Comment on the morphology of the erythrocytes.
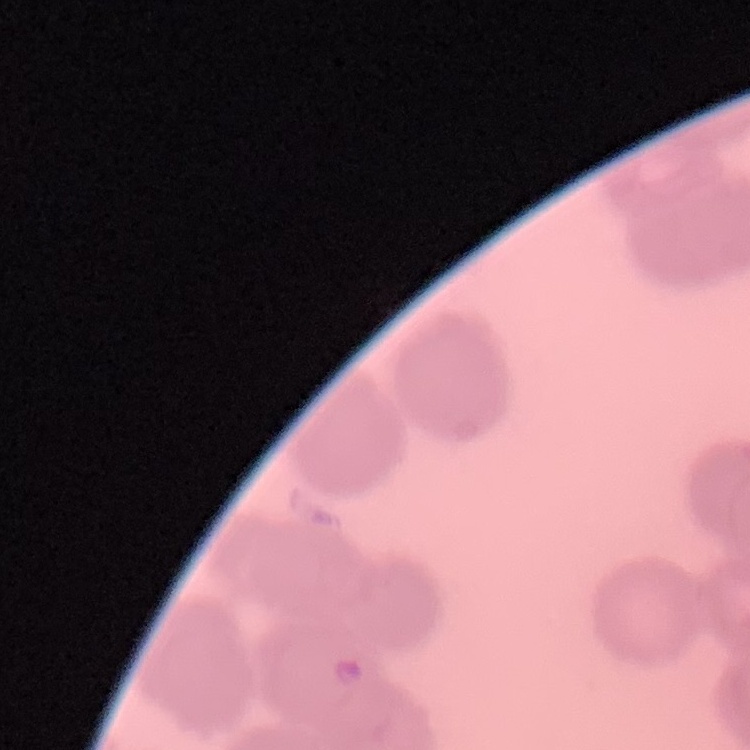
Rouleaux formation.

Summary:
  - Preparation: thin blood film
  - Stain: Field's or Giemsa
  - Image type: square crop of a larger photomicrograph